Assess this cell for malaria.
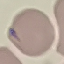

Uninfected.

image type = cell patch, automatically extracted from a larger field of view and resized to 64 × 64 pixels
capture = smartphone through the microscope eyepiece
stain = Giemsa
preparation = thin blood smear